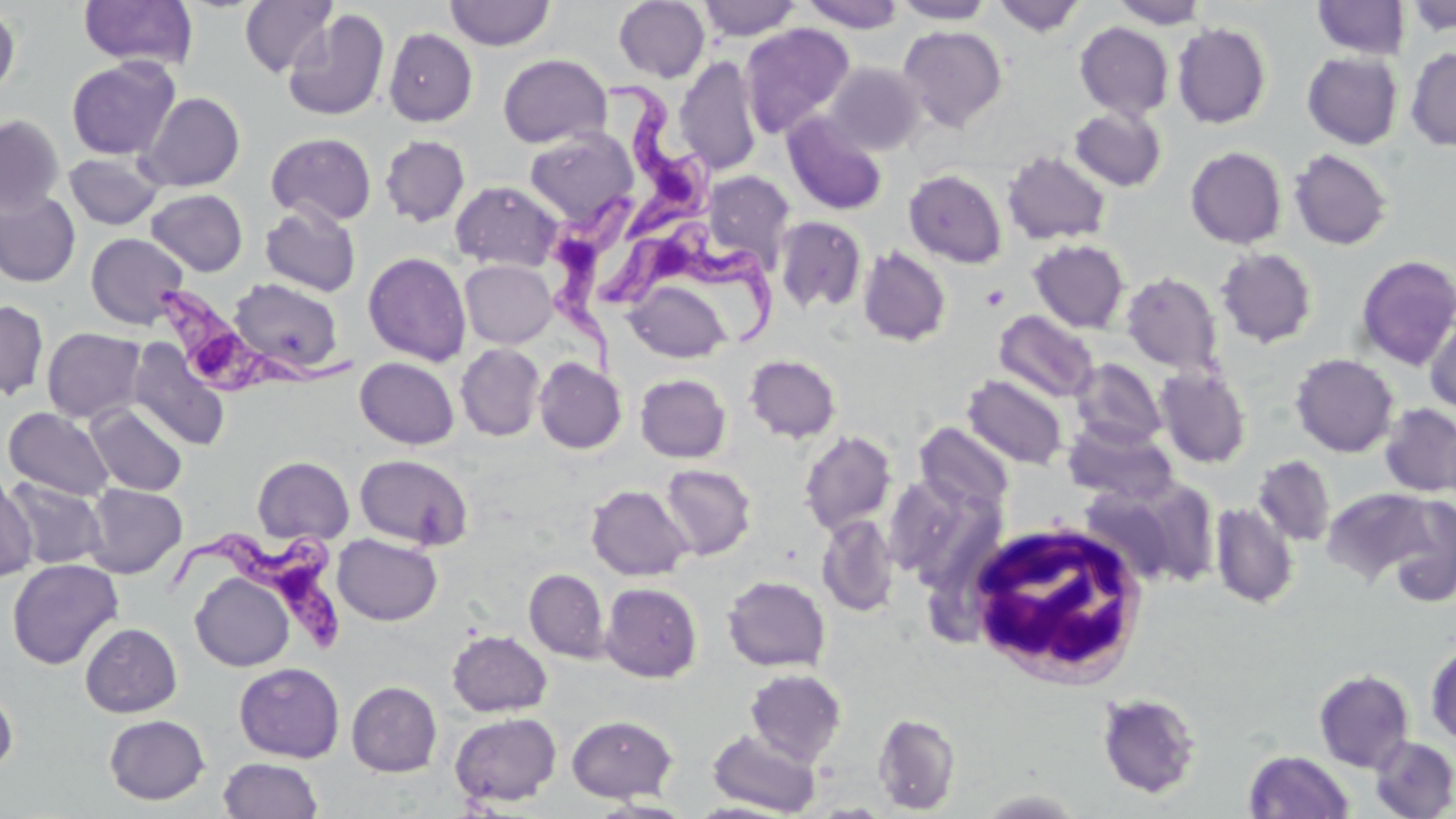

slide-level diagnosis = Trypanosoma brucei
magnification = 1000x
uninfected red blood cell locations = approximate bounding boxes as (x1, y1, x2, y2) in pixels: (239, 0, 338, 78), (697, 0, 802, 41), (799, 0, 905, 33), (892, 0, 996, 24), (991, 0, 1087, 37), (1111, 0, 1207, 29), (1311, 0, 1410, 59), (1405, 0, 1456, 36), (79, 1, 198, 69), (444, 1, 555, 50), (613, 1, 710, 83), (0, 5, 20, 100), (283, 8, 390, 122), (1074, 22, 1174, 121), (1172, 22, 1272, 128), (740, 23, 855, 139), (897, 25, 1008, 132), (384, 28, 477, 126), (1405, 47, 1456, 152), (1302, 52, 1403, 150), (498, 54, 612, 148), (66, 56, 180, 160), (675, 57, 763, 176), (823, 62, 926, 155), (137, 92, 245, 192), (1068, 106, 1167, 192), (782, 112, 888, 215), (0, 115, 64, 215), (523, 129, 638, 227), (266, 132, 377, 226), (380, 135, 470, 226), (1185, 146, 1287, 249), (1288, 148, 1393, 251), (1001, 150, 1111, 246), (64, 152, 164, 230), (904, 169, 1007, 268), (702, 170, 796, 269), (450, 180, 563, 272), (0, 189, 80, 288), (146, 189, 248, 276), (260, 204, 361, 296), (774, 216, 867, 313), (86, 232, 189, 329), (1028, 239, 1129, 334), (857, 246, 952, 347), (1215, 247, 1318, 348), (363, 251, 471, 366), (1355, 254, 1456, 370), (460, 259, 557, 348), (1121, 271, 1223, 375), (229, 277, 344, 375), (627, 280, 732, 364), (0, 300, 49, 401), (994, 310, 1099, 403), (1424, 310, 1456, 415), (41, 327, 146, 423), (127, 338, 231, 452), (456, 343, 545, 441), (1290, 353, 1399, 457), (744, 354, 841, 444), (355, 357, 459, 449), (534, 358, 627, 454), (1070, 358, 1167, 450), (1155, 366, 1251, 469), (635, 374, 731, 463), (963, 374, 1069, 469), (86, 403, 187, 495), (1378, 403, 1456, 498), (4, 407, 114, 501), (1062, 422, 1178, 504), (915, 423, 1014, 516), (799, 430, 897, 534), (355, 454, 473, 550), (1252, 455, 1336, 546), (252, 456, 354, 546), (659, 464, 756, 560), (885, 467, 968, 577), (0, 470, 38, 582), (4, 477, 108, 570), (1127, 478, 1220, 587), (83, 484, 187, 579), (586, 485, 693, 581), (1079, 485, 1184, 586), (1322, 487, 1438, 585), (1380, 496, 1456, 606), (1210, 502, 1299, 609), (816, 514, 898, 616), (332, 533, 442, 625), (7, 559, 123, 670), (524, 569, 609, 662), (191, 573, 294, 671), (722, 575, 831, 672), (734, 576, 839, 766), (599, 582, 702, 683), (80, 623, 182, 717), (447, 630, 552, 717), (1425, 643, 1456, 745), (234, 662, 344, 763), (744, 668, 847, 766), (1313, 669, 1415, 773), (0, 680, 18, 776), (346, 681, 442, 776), (1095, 692, 1203, 800), (450, 712, 561, 807), (873, 713, 961, 815), (104, 714, 210, 805), (566, 714, 678, 802), (708, 729, 820, 815), (1369, 735, 1456, 818), (1243, 750, 1355, 818), (218, 757, 324, 818), (686, 802, 792, 818)
field of view = one of a larger specimen
stain = May-Grünwald-Giemsa
Trypanosoma brucei locations = approximate bounding boxes as (x1, y1, x2, y2) in pixels: (598, 77, 716, 243), (546, 183, 647, 388), (601, 224, 780, 349), (155, 279, 355, 403), (159, 518, 357, 656)
preparation = thin blood film
modality = light microscopy
image size = 1456×819 pixels
white blood cell locations = approximate bounding boxes as (x1, y1, x2, y2) in pixels: (965, 519, 1152, 687)